Name the parasite shown.
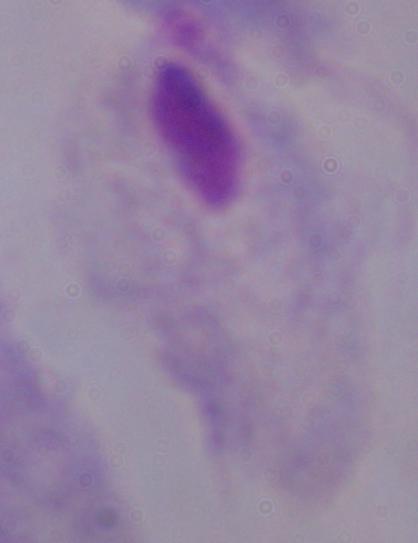

This is a trichomonad.

Micrograph. 1000x magnification.